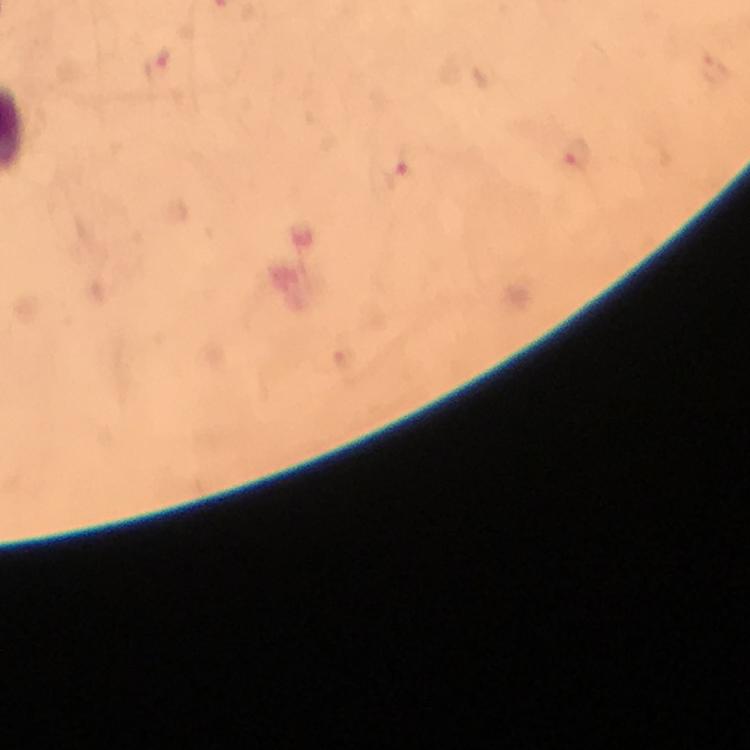

Approximate centers as [x, y] in pixels. Malaria parasite locations: [156, 66], [577, 158], [402, 169]. Immersion oil applied. 100x magnification. Smartphone photograph taken through a microscope. From a malaria diagnostic workup. Image is 750×750 pixels. Thick blood film. Giemsa-stained preparation. A crop from one field of view.